State the blood parasite species.
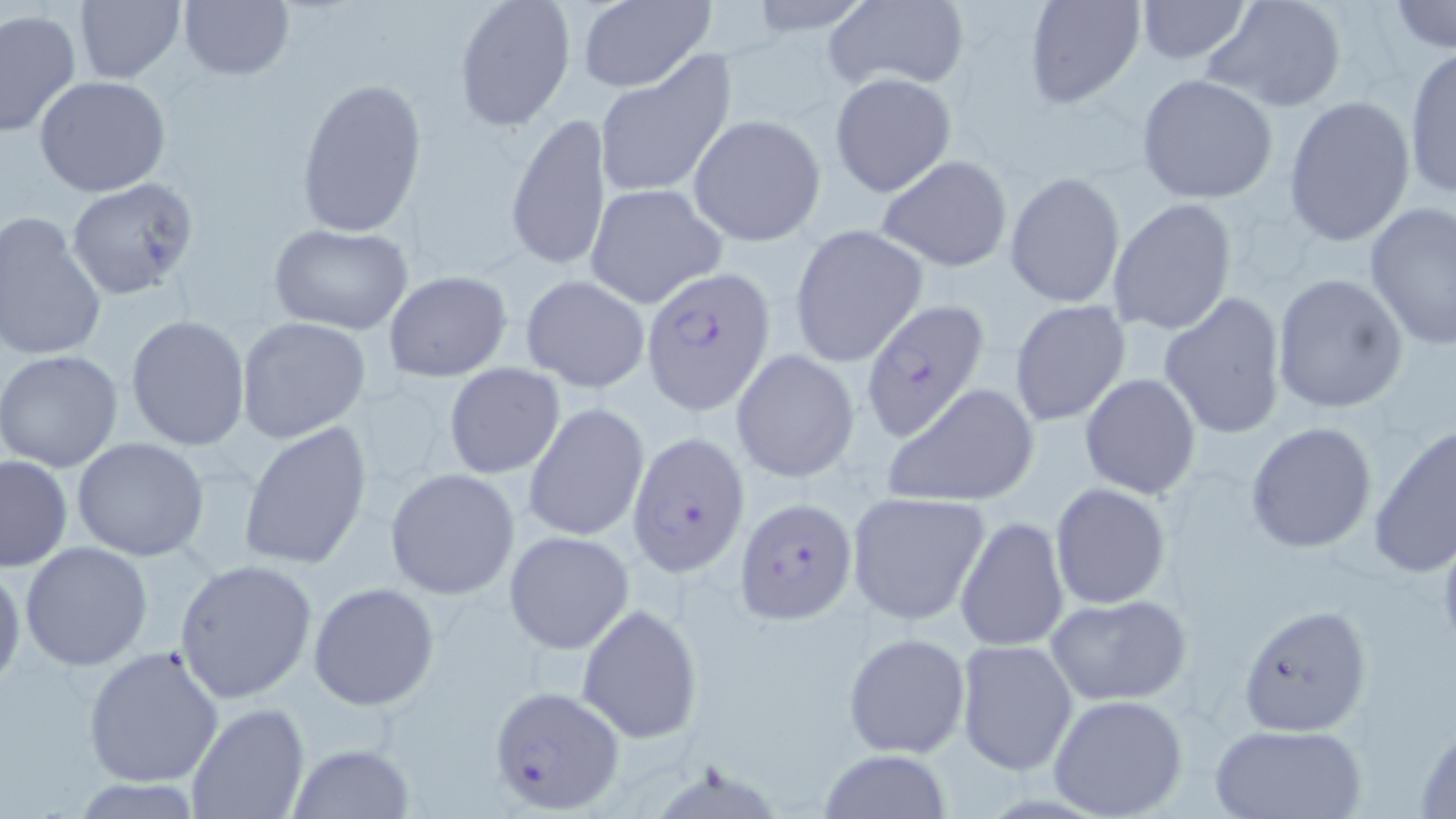
Plasmodium falciparum.

Summary:
  - Coordinate format: approximate bounding boxes as (x1,y1)-(x2,y2) corner pairs in pixels
  - Plasmodium falciparum-infected red blood cell locations: (641,270)-(777,414), (860,301)-(993,440), (626,430)-(752,579), (733,495)-(858,621), (489,683)-(626,813)
  - Uninfected red blood cell locations: (176,0)-(296,81), (454,0)-(577,132), (1021,0)-(1146,109), (1132,0)-(1256,64), (1200,0)-(1350,114), (73,1)-(185,83), (575,1)-(714,91), (823,1)-(969,91), (1387,2)-(1455,53), (0,9)-(80,139), (1402,48)-(1456,202), (593,52)-(737,202), (830,72)-(957,198), (1135,75)-(1279,206), (34,76)-(172,197), (295,76)-(428,238), (1283,94)-(1417,247), (503,112)-(613,273), (687,114)-(825,246), (874,154)-(1013,273), (1004,171)-(1126,308), (66,178)-(200,300), (585,184)-(727,309), (1107,197)-(1238,337), (1364,202)-(1456,350), (0,212)-(108,363), (267,223)-(414,335), (791,224)-(929,367), (383,270)-(512,382), (1269,273)-(1409,415), (521,275)-(651,393), (1158,291)-(1289,440), (1008,300)-(1131,428), (125,314)-(251,451), (236,317)-(371,442), (0,350)-(124,473), (732,350)-(860,485), (443,363)-(565,478), (1080,374)-(1201,499), (882,383)-(1040,508), (524,403)-(649,543), (1245,421)-(1378,553), (239,422)-(372,570), (1369,423)-(1456,579), (72,437)-(209,560), (0,453)-(72,572), (385,467)-(521,599), (1050,483)-(1173,609), (846,491)-(991,625), (954,516)-(1069,651), (504,530)-(635,654), (21,541)-(152,669), (172,559)-(318,704), (0,561)-(26,691), (307,581)-(440,711), (1045,593)-(1192,707), (1239,603)-(1370,736), (577,604)-(704,743), (842,631)-(971,759), (955,641)-(1078,776), (82,644)-(225,788), (1047,693)-(1188,819), (184,702)-(311,818), (1412,718)-(1456,818), (1209,723)-(1368,819), (286,741)-(414,817), (815,749)-(953,819), (69,778)-(205,817)
  - Magnification: 1000x
  - Field of view: single
  - Stain: May-Grünwald-Giemsa
  - Image size: 1456×819 pixels
  - Preparation: thin blood smear
  - Modality: light microscopy